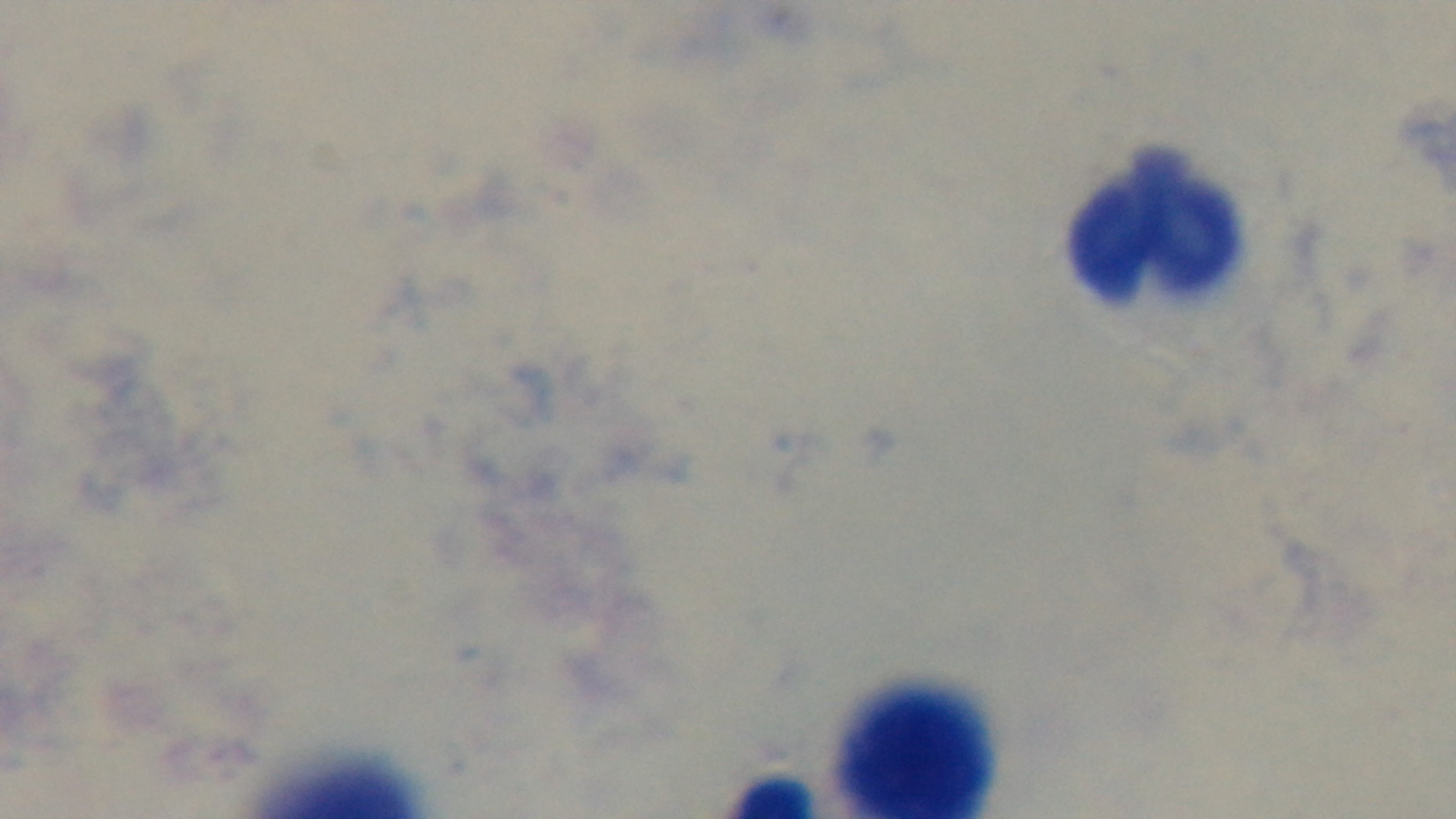

preparation = thick
stain = Giemsa
malaria status = negative
field of view = single
modality = light microscopy
objective = 100x oil immersion
capture = mounted 4K digital camera